Comment on the morphology of the erythrocytes.
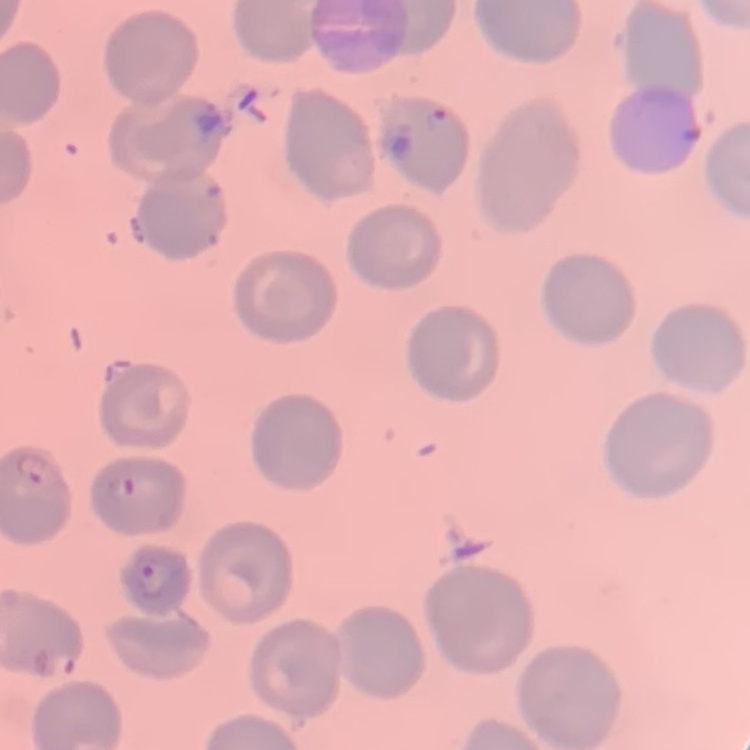
No rouleaux formation.

Square crop of a larger photomicrograph. Field's or Giemsa stain. Thin blood film.